Locate every Plasmodium parasite.
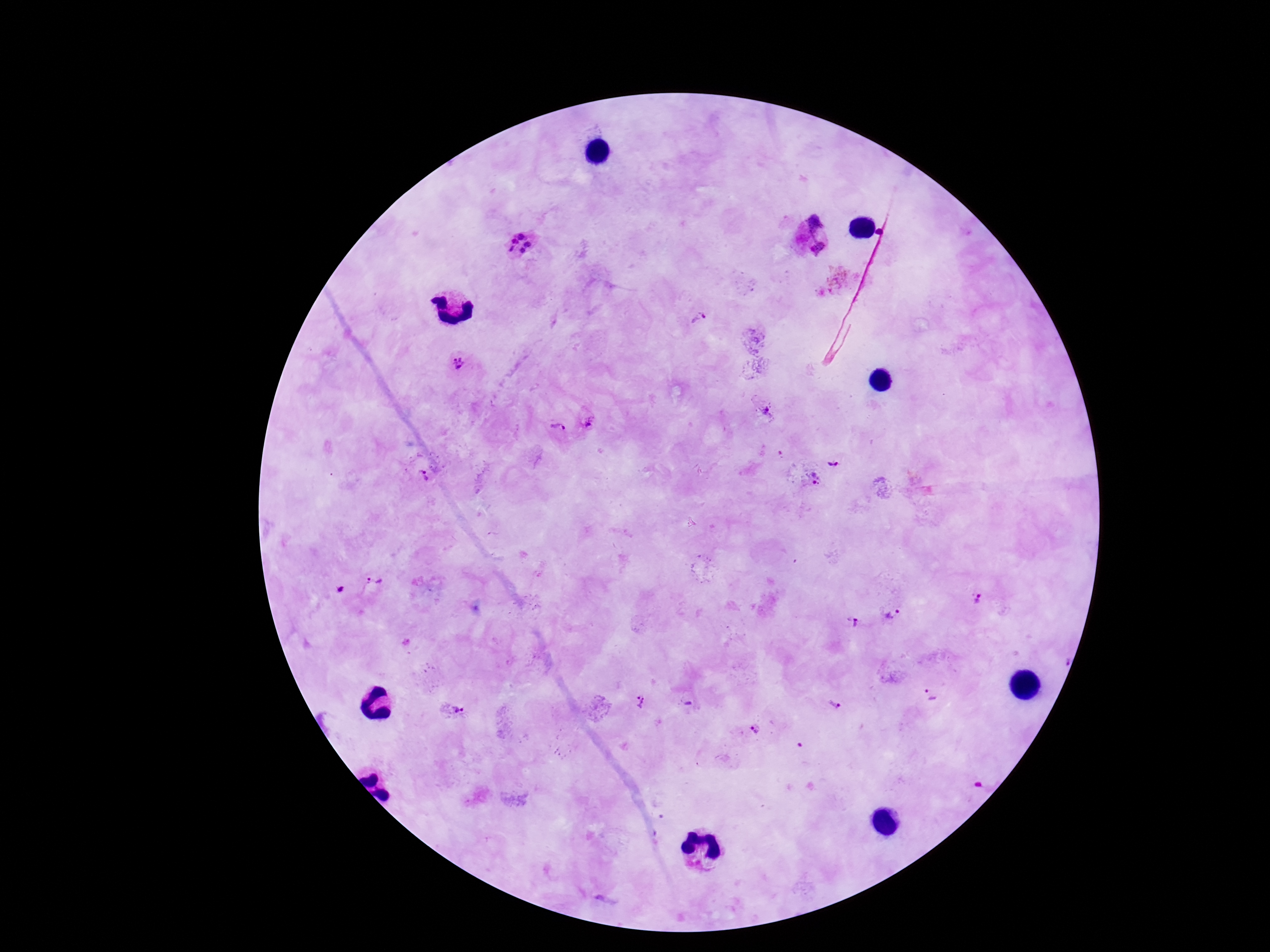
Approximate object centers, in pixels from the top-left corner.
Plasmodium parasites: (x=813, y=235), (x=520, y=244), (x=698, y=320), (x=460, y=365), (x=768, y=410), (x=589, y=421), (x=557, y=428), (x=834, y=463), (x=425, y=473), (x=813, y=479), (x=374, y=583), (x=339, y=591), (x=978, y=598), (x=892, y=612), (x=855, y=623), (x=931, y=695), (x=690, y=703), (x=834, y=703), (x=639, y=704), (x=449, y=710), (x=756, y=728).

magnification = 100x
stain = Giemsa
capture = smartphone camera through the microscope eyepiece
patient malaria status = infected
image size = 1270×952 pixels
preparation = thick blood smear
field of view = one from this slide